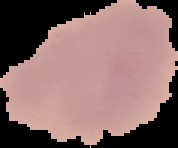
{
  "image_size": "178×148 pixels",
  "preparation": "thin blood film",
  "malaria_status": "uninfected",
  "image_type": "segmented cell region on a black background"
}